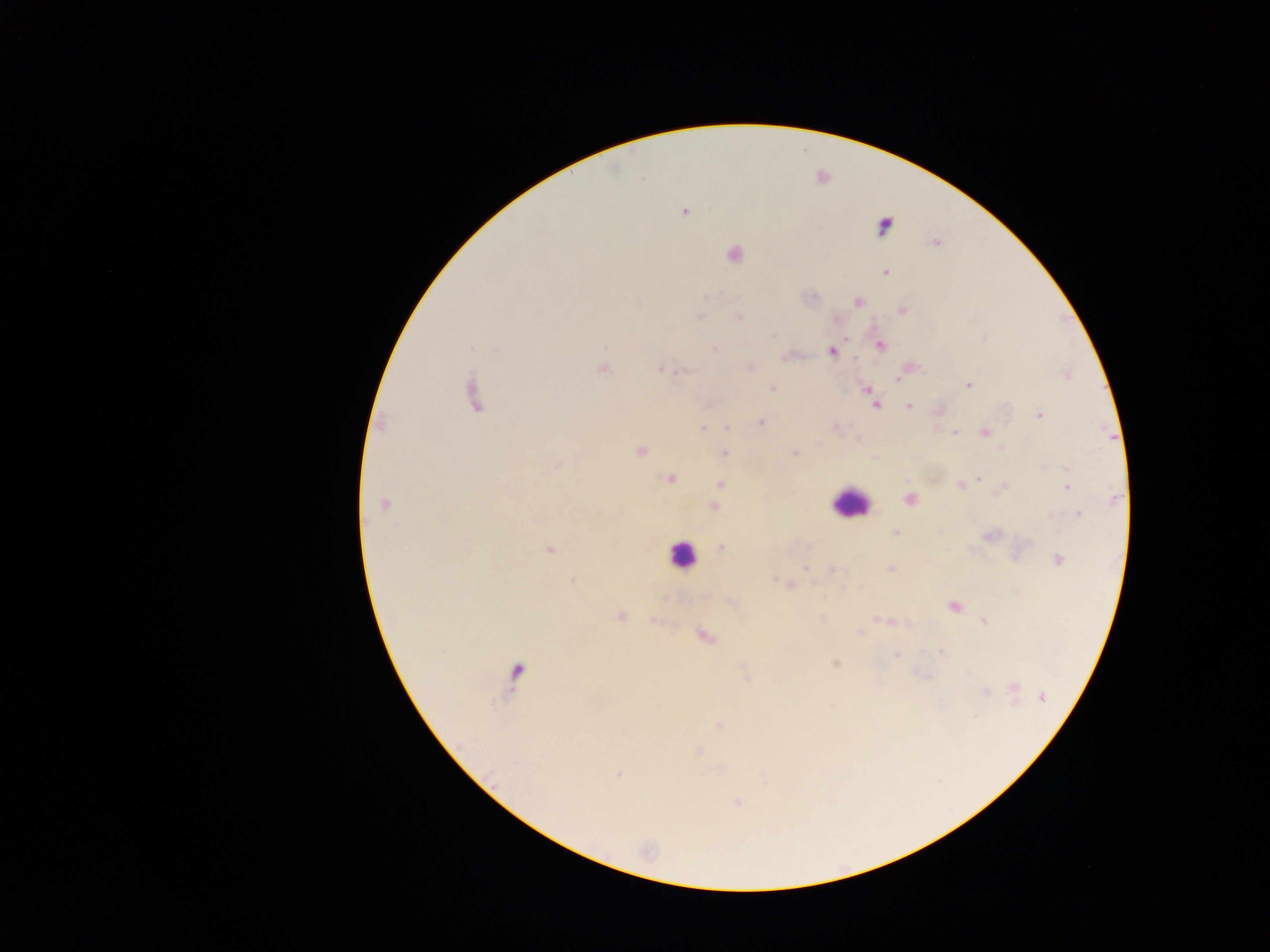

Approximate centers as [x, y] in pixels.
Summary:
  - Leukocyte locations: [849, 503], [681, 555], [516, 671]
  - Malaria parasite locations: [684, 211], [884, 225], [936, 242], [734, 254], [886, 271], [858, 302], [902, 310], [738, 316], [700, 317], [774, 335], [845, 339], [881, 346], [831, 351], [784, 357], [854, 358], [749, 366], [603, 369], [660, 370], [899, 378], [969, 385], [773, 388], [867, 388], [473, 395], [876, 405], [909, 406], [1039, 415], [760, 422], [727, 427], [701, 429], [985, 432], [954, 433], [858, 439], [819, 445], [1003, 448], [640, 451], [724, 453], [794, 453], [1044, 466], [1065, 469], [979, 478], [670, 479], [720, 484], [960, 484], [1067, 487], [1002, 488], [716, 498], [1115, 498], [909, 499], [384, 505], [713, 507], [1079, 515], [1052, 516], [896, 532], [990, 535], [809, 546], [721, 548], [550, 549], [1058, 560], [805, 568], [891, 569], [832, 570], [773, 578], [572, 580], [789, 584], [953, 606], [621, 616], [822, 619], [877, 619], [985, 621], [859, 633], [705, 636], [941, 652], [896, 655], [835, 664], [746, 675], [1014, 688], [986, 692], [1042, 697], [975, 716], [719, 725], [698, 752], [618, 775], [736, 802]
  - Capture: mobile-phone photograph through a microscope
  - Image size: 1270×952 pixels
  - Preparation: thick blood smear
  - Country: Ghana
  - Field of view: single